Assess the morphology of the red blood cells.
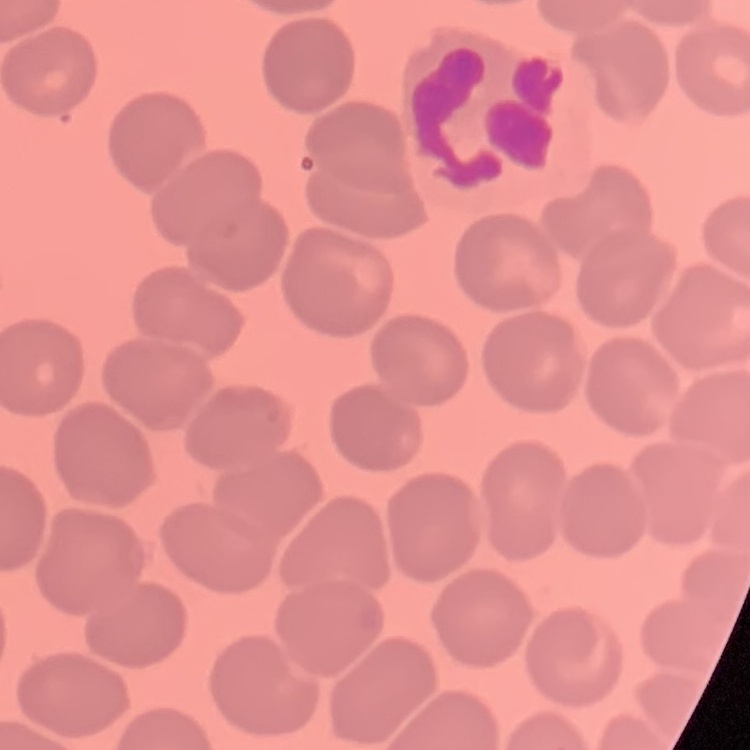
They show no rouleaux formation.

Summary:
  - Stain: Field's or Giemsa
  - Preparation: thin peripheral smear
  - Image type: square crop of a larger photomicrograph